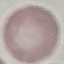
Malaria status: uninfected. Thin blood smear. Automatically extracted cell patch, resized to 64 × 64 pixels. Giemsa stain. Photographed with a smartphone camera at the microscope eyepiece.